Report the malaria status of this cell.
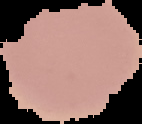

It is uninfected.

From a thin blood film. Segmented cell region on a black background. Image is 142×124 pixels.